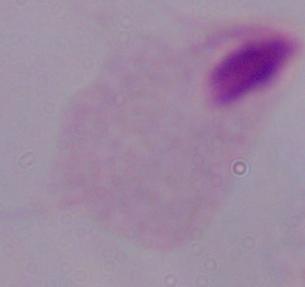

modality = photomicrograph
magnification = 1000x
identification = trichomonad